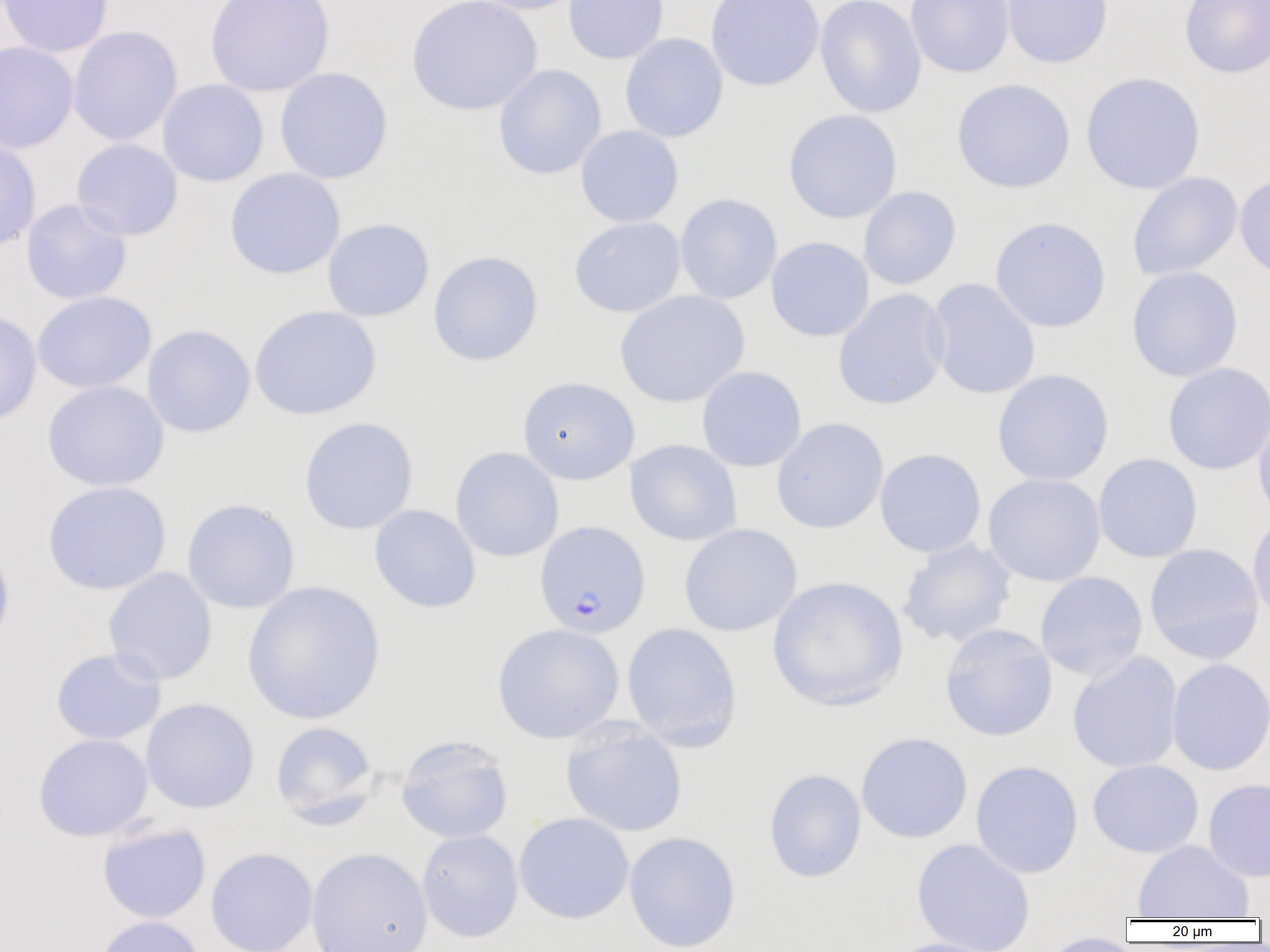

slide-level diagnosis = Plasmodium falciparum
image size = 1270×952 pixels
modality = light microscopy
uninfected red blood cell locations = approximate bounding boxes as (x1, y1, x2, y2) in pixels: (0, 0, 114, 58), (204, 0, 335, 97), (406, 0, 543, 116), (469, 0, 587, 15), (563, 0, 669, 64), (705, 0, 825, 91), (815, 0, 927, 118), (905, 0, 1015, 78), (1002, 0, 1114, 68), (1179, 0, 1270, 78), (68, 25, 182, 146), (620, 33, 728, 142), (0, 41, 79, 153), (494, 64, 607, 179), (274, 67, 393, 184), (1080, 72, 1205, 195), (951, 78, 1075, 193), (157, 79, 269, 187), (783, 109, 903, 224), (575, 125, 684, 227), (0, 137, 41, 253), (71, 138, 183, 241), (224, 168, 345, 279), (1127, 172, 1243, 281), (1234, 172, 1270, 285), (858, 186, 961, 290), (675, 193, 782, 304), (20, 199, 132, 305), (569, 216, 686, 317), (990, 216, 1112, 333), (322, 218, 434, 321), (766, 237, 874, 342), (428, 251, 543, 366), (1126, 266, 1243, 382), (926, 278, 1041, 400), (833, 289, 951, 410), (32, 291, 156, 393), (614, 291, 750, 408), (249, 305, 381, 420), (0, 309, 42, 428), (142, 324, 256, 438), (1162, 362, 1270, 475), (697, 366, 806, 472), (992, 369, 1114, 486), (517, 376, 639, 485), (42, 381, 169, 491), (1253, 408, 1270, 527), (298, 416, 418, 534), (771, 417, 888, 534), (625, 439, 742, 546), (450, 447, 564, 562), (875, 448, 986, 558), (1093, 453, 1203, 563), (983, 473, 1105, 586), (42, 481, 171, 594), (181, 498, 300, 614), (369, 505, 481, 613), (1247, 512, 1270, 628), (678, 523, 802, 637), (0, 536, 15, 655), (896, 539, 1017, 648), (1144, 543, 1265, 665), (103, 568, 217, 685), (1035, 571, 1148, 681), (768, 576, 908, 711), (242, 581, 386, 725), (621, 622, 742, 751), (492, 623, 624, 744), (940, 623, 1057, 741), (50, 647, 166, 745), (1067, 651, 1183, 773), (1166, 658, 1270, 776), (140, 698, 259, 813), (271, 721, 380, 828), (561, 722, 687, 837), (855, 732, 973, 843), (33, 733, 153, 842), (395, 735, 513, 844), (1087, 759, 1203, 858), (970, 760, 1084, 878), (763, 768, 866, 883), (1203, 778, 1270, 882), (513, 812, 634, 924), (96, 823, 211, 923), (417, 830, 523, 942), (623, 831, 741, 952), (911, 838, 1036, 952), (1133, 840, 1254, 920), (205, 847, 318, 952), (306, 847, 433, 952), (93, 915, 206, 952), (1039, 932, 1144, 952), (881, 937, 1009, 952)
magnification = 1000x
preparation = thin blood film
field of view = single
Plasmodium falciparum-infected red blood cell locations = approximate bounding boxes as (x1, y1, x2, y2) in pixels: (534, 520, 650, 638)